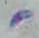

{
  "magnification": "1000x",
  "identification": "Toxoplasma gondii",
  "modality": "micrograph"
}